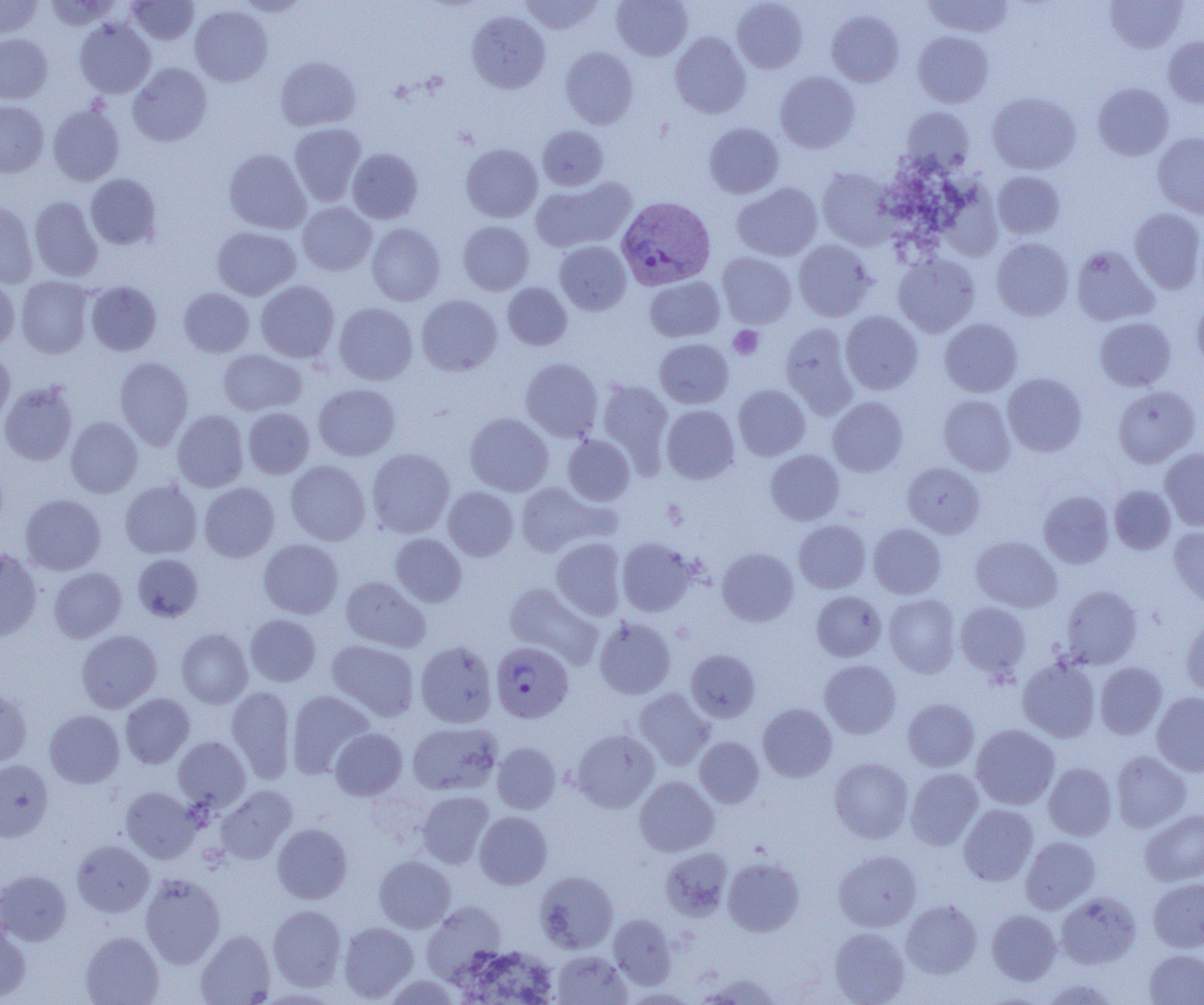

Approximate bounding boxes as (x1,y1)-(x2,y2) corner pairs in pixels. Uninfected red blood cell locations: (43,0)-(120,31), (127,0)-(199,45), (235,0)-(311,17), (520,0)-(603,34), (611,0)-(693,61), (923,0)-(1014,37), (1104,0)-(1187,53), (0,1)-(44,39), (732,1)-(807,73), (190,5)-(272,86), (827,9)-(904,87), (467,11)-(550,93), (75,18)-(155,98), (913,31)-(994,107), (0,33)-(53,103), (670,33)-(751,118), (1163,37)-(1204,107), (561,47)-(638,129), (275,57)-(361,131), (128,62)-(212,146), (775,71)-(860,152), (1092,83)-(1174,160), (987,92)-(1081,174), (0,100)-(49,177), (48,104)-(125,186), (901,107)-(974,175), (704,122)-(784,198), (288,123)-(366,206), (537,125)-(608,191), (1152,132)-(1204,218), (461,144)-(542,222), (223,148)-(311,234), (347,148)-(423,223), (817,168)-(898,250), (992,170)-(1065,239), (85,173)-(161,250), (531,177)-(636,254), (732,182)-(822,261), (29,196)-(103,281), (0,200)-(38,288), (297,202)-(376,275), (1129,208)-(1204,293), (458,220)-(534,295), (366,223)-(445,305), (211,226)-(300,300), (991,238)-(1074,320), (793,239)-(875,321), (555,241)-(631,315), (1071,246)-(1158,326), (717,252)-(796,327), (893,254)-(980,337), (0,276)-(19,352), (16,276)-(95,358), (645,277)-(724,342), (256,280)-(339,363), (85,281)-(162,355), (502,282)-(572,350), (178,287)-(255,357), (417,295)-(502,376), (1192,299)-(1204,372), (334,302)-(418,385), (840,310)-(923,394), (1094,317)-(1176,391), (939,318)-(1022,397), (780,323)-(858,417), (655,338)-(733,408), (0,349)-(15,425), (218,349)-(307,416), (115,357)-(193,449), (521,357)-(603,441), (1003,373)-(1086,456), (597,379)-(673,469), (0,381)-(78,466), (313,384)-(400,460), (733,385)-(810,460), (1112,386)-(1201,468), (938,395)-(1015,476), (828,397)-(908,476), (661,405)-(739,483), (243,407)-(314,478), (172,410)-(249,492), (465,412)-(553,496), (65,416)-(142,497), (563,435)-(635,505), (367,448)-(455,537), (1160,448)-(1204,530), (765,450)-(844,525), (286,460)-(370,545), (903,462)-(985,538), (120,479)-(202,558), (199,482)-(279,562), (515,482)-(608,556), (1109,485)-(1175,554), (443,486)-(518,561), (1039,491)-(1114,568), (20,494)-(106,575), (793,520)-(871,593), (869,524)-(946,599), (1169,526)-(1204,609), (390,533)-(466,606), (970,535)-(1062,611), (258,538)-(343,618), (551,538)-(626,619), (617,538)-(696,616), (717,547)-(799,626), (0,549)-(42,644), (133,554)-(203,622), (48,567)-(127,643), (340,576)-(430,652), (504,582)-(603,669), (1060,585)-(1142,669), (811,591)-(885,661), (884,594)-(961,677), (954,602)-(1031,680), (245,614)-(321,687), (1181,614)-(1204,697), (594,616)-(676,700), (176,629)-(252,708), (76,630)-(162,713), (327,639)-(419,721), (416,640)-(497,728), (686,649)-(760,722), (1017,657)-(1100,742), (819,660)-(901,739), (1094,662)-(1167,739), (227,685)-(296,782), (0,688)-(32,769), (634,688)-(715,770), (286,691)-(375,778), (1152,692)-(1204,776), (121,693)-(194,768), (903,698)-(980,771), (758,703)-(837,781), (44,710)-(124,788), (408,721)-(502,795), (971,724)-(1060,809), (330,728)-(407,800), (571,730)-(659,812), (173,736)-(250,811), (694,736)-(764,807), (492,742)-(561,814), (1111,750)-(1192,832), (829,757)-(913,843), (0,760)-(53,841), (1043,762)-(1117,840), (906,768)-(983,850), (634,776)-(719,856), (215,786)-(296,863), (121,787)-(200,863), (417,791)-(494,868), (958,804)-(1038,886), (1140,809)-(1204,886), (474,811)-(552,889), (272,823)-(352,904), (1020,836)-(1100,913), (71,840)-(154,917), (660,847)-(733,920), (834,850)-(921,931), (374,855)-(455,933), (723,857)-(804,936), (0,870)-(72,946), (534,870)-(618,953), (140,873)-(225,968), (1148,877)-(1204,952), (1056,892)-(1140,969), (901,900)-(982,978), (421,902)-(508,983), (267,905)-(347,991), (987,909)-(1061,984), (608,913)-(676,988), (338,922)-(418,1002), (0,925)-(31,1002), (829,927)-(909,1004), (196,930)-(275,1004), (81,931)-(164,1005), (454,945)-(559,1004), (1144,949)-(1204,1004), (552,950)-(631,1004), (695,973)-(782,1004), (383,974)-(462,1005), (1040,978)-(1119,1004), (622,988)-(699,1004). Platelet locations: (729,326)-(763,359). Plasmodium vivax-infected red blood cell locations: (616,197)-(715,291), (491,641)-(573,723). Slide-level diagnosis: Plasmodium vivax. Single field of view. Light microscopy. Thin blood smear. Image is 1204×1005 pixels. 1000x magnification.